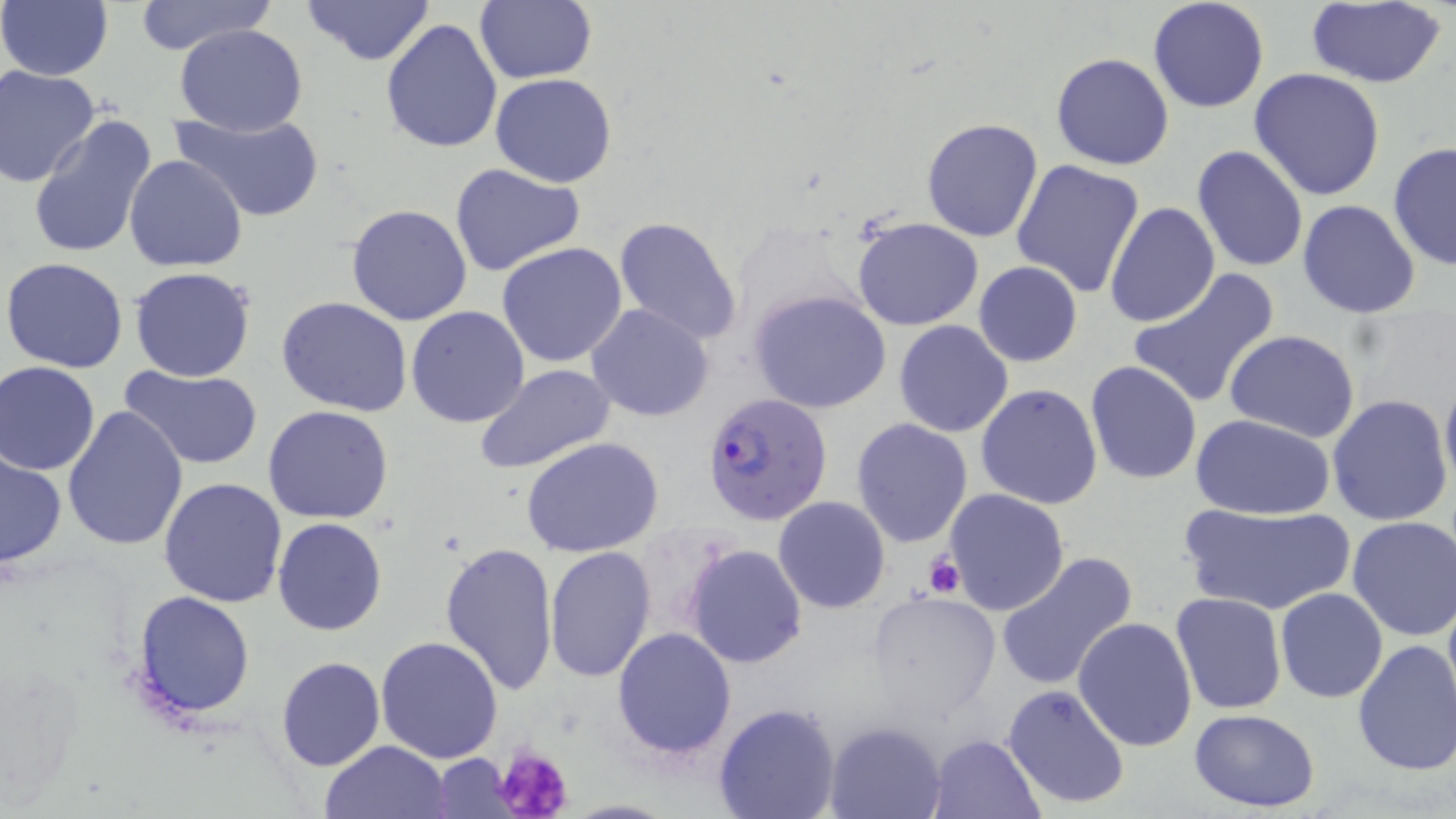

Summary:
  - Coordinate format: approximate bounding boxes as [x1, y1, x2, y2] in pixels
  - Uninfected red blood cell locations: [303, 0, 435, 67], [476, 0, 596, 84], [1148, 0, 1270, 114], [1302, 0, 1449, 88], [131, 1, 276, 57], [0, 2, 113, 80], [381, 18, 504, 155], [174, 23, 307, 136], [1051, 52, 1176, 170], [1, 66, 102, 186], [1249, 67, 1386, 201], [490, 74, 618, 188], [171, 108, 326, 223], [29, 115, 159, 260], [920, 117, 1044, 243], [1388, 140, 1456, 272], [1191, 145, 1308, 272], [125, 154, 248, 272], [1010, 158, 1146, 298], [449, 161, 585, 277], [1296, 199, 1420, 318], [1102, 201, 1219, 328], [346, 204, 474, 326], [612, 216, 743, 346], [851, 216, 985, 331], [497, 242, 629, 368], [2, 256, 130, 373], [973, 262, 1083, 367], [129, 266, 257, 382], [1127, 270, 1280, 409], [749, 288, 891, 414], [277, 296, 413, 417], [587, 303, 713, 422], [406, 305, 529, 428], [895, 321, 1014, 437], [1224, 330, 1362, 443], [1084, 360, 1203, 485], [0, 362, 101, 474], [474, 364, 616, 477], [120, 365, 262, 472], [1440, 371, 1456, 496], [975, 383, 1103, 509], [1327, 394, 1453, 525], [61, 404, 188, 550], [262, 404, 394, 524], [1190, 414, 1337, 521], [852, 419, 973, 548], [520, 436, 665, 556], [1, 451, 67, 570], [158, 477, 289, 607], [943, 488, 1070, 615], [773, 496, 890, 613], [1179, 500, 1354, 617], [1346, 516, 1456, 641], [274, 517, 387, 635], [439, 541, 558, 695], [683, 542, 808, 669], [544, 547, 658, 684], [994, 551, 1139, 692], [1274, 587, 1388, 704], [132, 590, 256, 719], [1171, 591, 1287, 714], [867, 594, 1000, 721], [1073, 616, 1198, 751], [612, 627, 738, 762], [375, 635, 503, 764], [1351, 637, 1456, 777], [276, 657, 385, 772], [1002, 685, 1132, 811], [714, 702, 840, 819], [1189, 709, 1322, 812], [824, 721, 947, 818], [926, 732, 1046, 819], [321, 740, 451, 818], [431, 755, 516, 816]
  - Platelet locations: [922, 552, 967, 597], [492, 743, 575, 819]
  - Plasmodium falciparum-infected red blood cell locations: [703, 392, 832, 525]
  - Slide-level diagnosis: Plasmodium falciparum
  - Image size: 1456×819 pixels
  - Magnification: 1000x
  - Stain: May-Grünwald-Giemsa
  - Field of view: single
  - Preparation: thin blood film
  - Modality: light microscopy